Locate every blood parasite and identify its species.
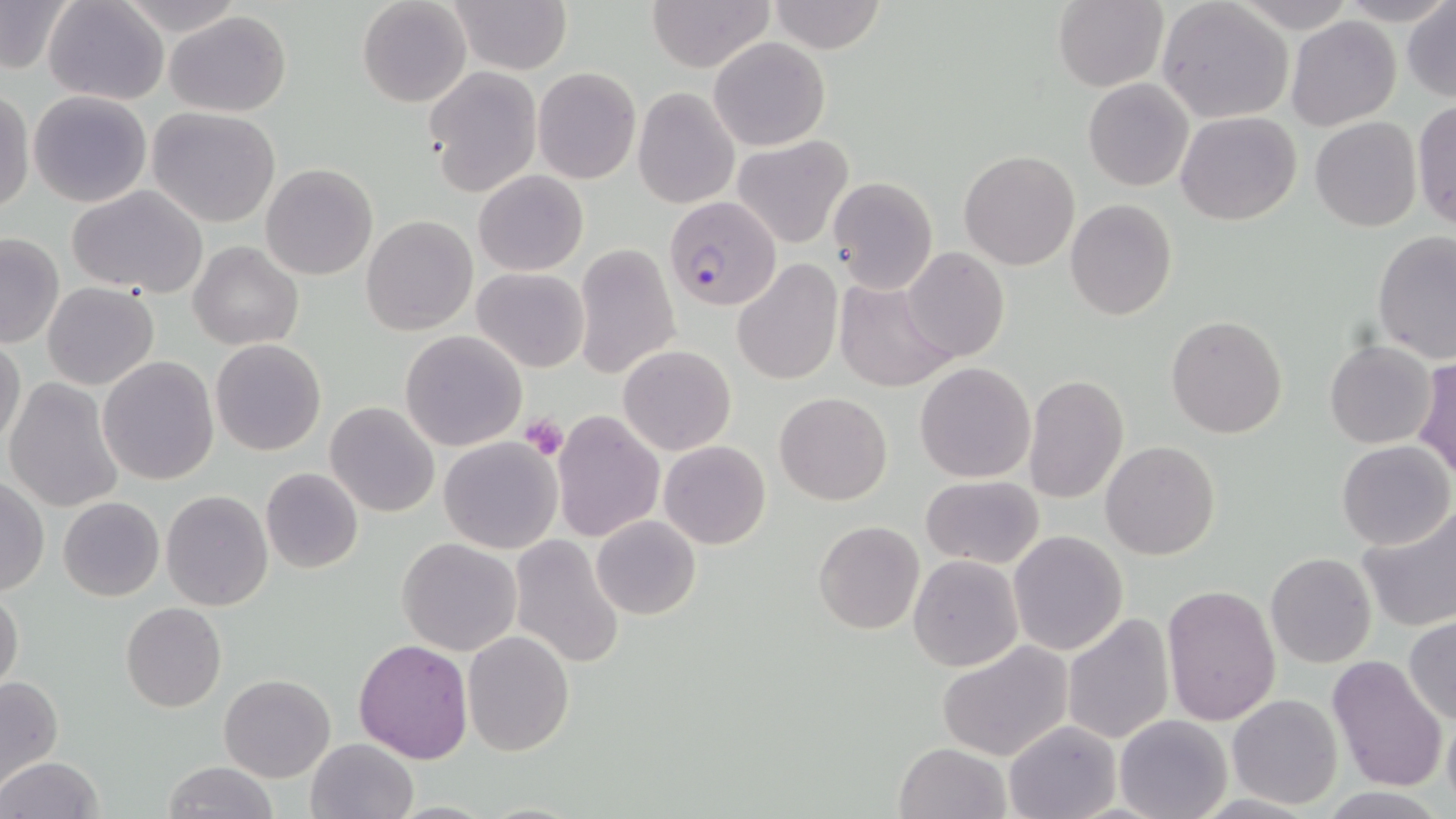

Approximate bounding boxes as (x1, y1, x2, y2) in pixels.
Plasmodium falciparum-infected red blood cells: (664, 196, 782, 312).
No Plasmodium ovale, Plasmodium malariae, Plasmodium vivax, Babesia divergens, or Trypanosoma brucei observed.

slide-level diagnosis = Plasmodium falciparum
modality = optical microscopy
image size = 1456×819 pixels
uninfected red blood cell locations = approximate bounding boxes as (x1, y1, x2, y2) in pixels: (42, 0, 169, 106), (113, 0, 246, 37), (357, 0, 471, 108), (446, 0, 571, 74), (647, 0, 777, 71), (767, 0, 887, 54), (0, 1, 74, 75), (1051, 1, 1168, 91), (1157, 1, 1294, 124), (1226, 2, 1364, 30), (1402, 2, 1456, 102), (163, 10, 292, 115), (1285, 15, 1401, 130), (708, 37, 831, 152), (423, 66, 542, 196), (533, 67, 640, 185), (1082, 78, 1195, 191), (0, 87, 34, 215), (632, 87, 740, 209), (27, 90, 154, 208), (1083, 92, 1297, 207), (1413, 99, 1455, 232), (147, 108, 281, 228), (1175, 111, 1302, 226), (1310, 116, 1423, 232), (732, 135, 854, 250), (959, 150, 1081, 270), (261, 163, 378, 280), (474, 170, 588, 276), (828, 176, 937, 293), (66, 186, 210, 296), (1065, 199, 1177, 321), (361, 215, 478, 336), (0, 231, 64, 350), (1372, 231, 1455, 364), (189, 242, 302, 351), (573, 245, 680, 378), (902, 248, 1009, 362), (733, 260, 843, 387), (472, 267, 589, 373), (832, 277, 955, 392), (43, 282, 159, 390), (1167, 316, 1288, 439), (400, 330, 528, 450), (0, 337, 27, 449), (210, 339, 326, 456), (1324, 339, 1437, 449), (619, 345, 736, 456), (98, 355, 219, 485), (1413, 357, 1456, 480), (915, 362, 1036, 483), (1024, 374, 1130, 506), (4, 377, 125, 514), (774, 392, 893, 506), (324, 402, 442, 518), (552, 410, 664, 541), (439, 436, 563, 554), (659, 440, 770, 550), (1100, 440, 1220, 559), (1336, 440, 1453, 551), (260, 468, 364, 572), (920, 475, 1045, 569), (0, 477, 49, 595), (159, 490, 274, 612), (59, 497, 165, 602), (1354, 505, 1456, 633), (591, 516, 701, 620), (814, 521, 924, 635), (1007, 530, 1128, 656), (397, 536, 522, 656), (508, 536, 627, 668), (1265, 552, 1376, 669), (908, 554, 1024, 672), (1162, 584, 1283, 728), (0, 587, 25, 696), (121, 601, 227, 713), (1062, 613, 1175, 744), (1404, 618, 1456, 727), (463, 630, 574, 755), (353, 637, 474, 764), (937, 640, 1073, 761), (1328, 656, 1449, 794), (219, 674, 335, 782), (0, 676, 62, 790), (1226, 694, 1343, 808), (1442, 708, 1456, 814), (1115, 713, 1232, 819), (1003, 719, 1124, 819), (305, 738, 420, 819), (893, 742, 1010, 819), (1, 756, 103, 819), (162, 761, 278, 818)
field of view = one of a larger specimen
platelet locations = approximate bounding boxes as (x1, y1, x2, y2) in pixels: (519, 414, 567, 459)
stain = May-Grünwald-Giemsa
preparation = thin blood film
magnification = 1000x